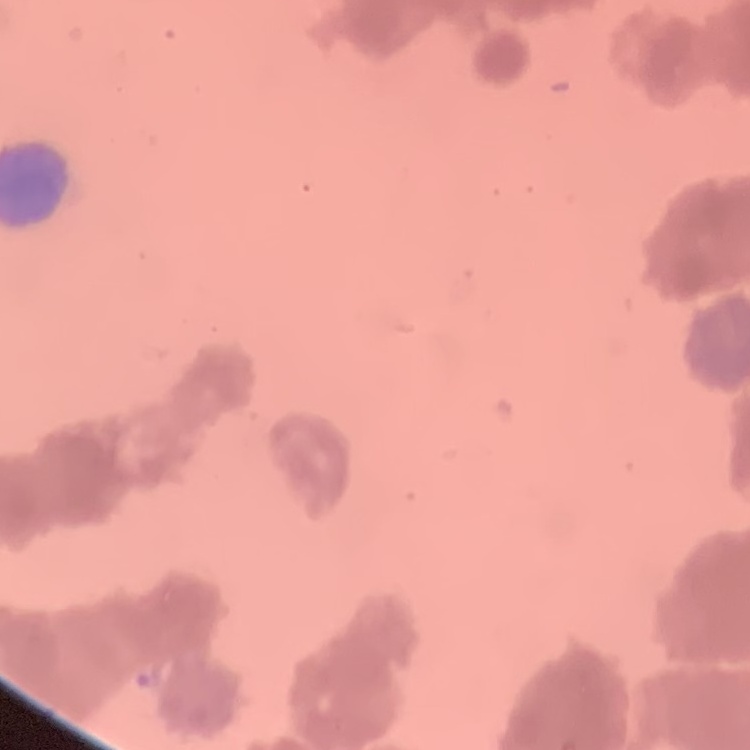

The red blood cells show rouleaux formation. Thin blood smear. Stained with either Field's or Giemsa. Square crop of a larger photomicrograph.